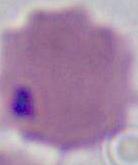

{
  "modality": "micrograph",
  "magnification": "1000x",
  "identification": "red blood cell"
}